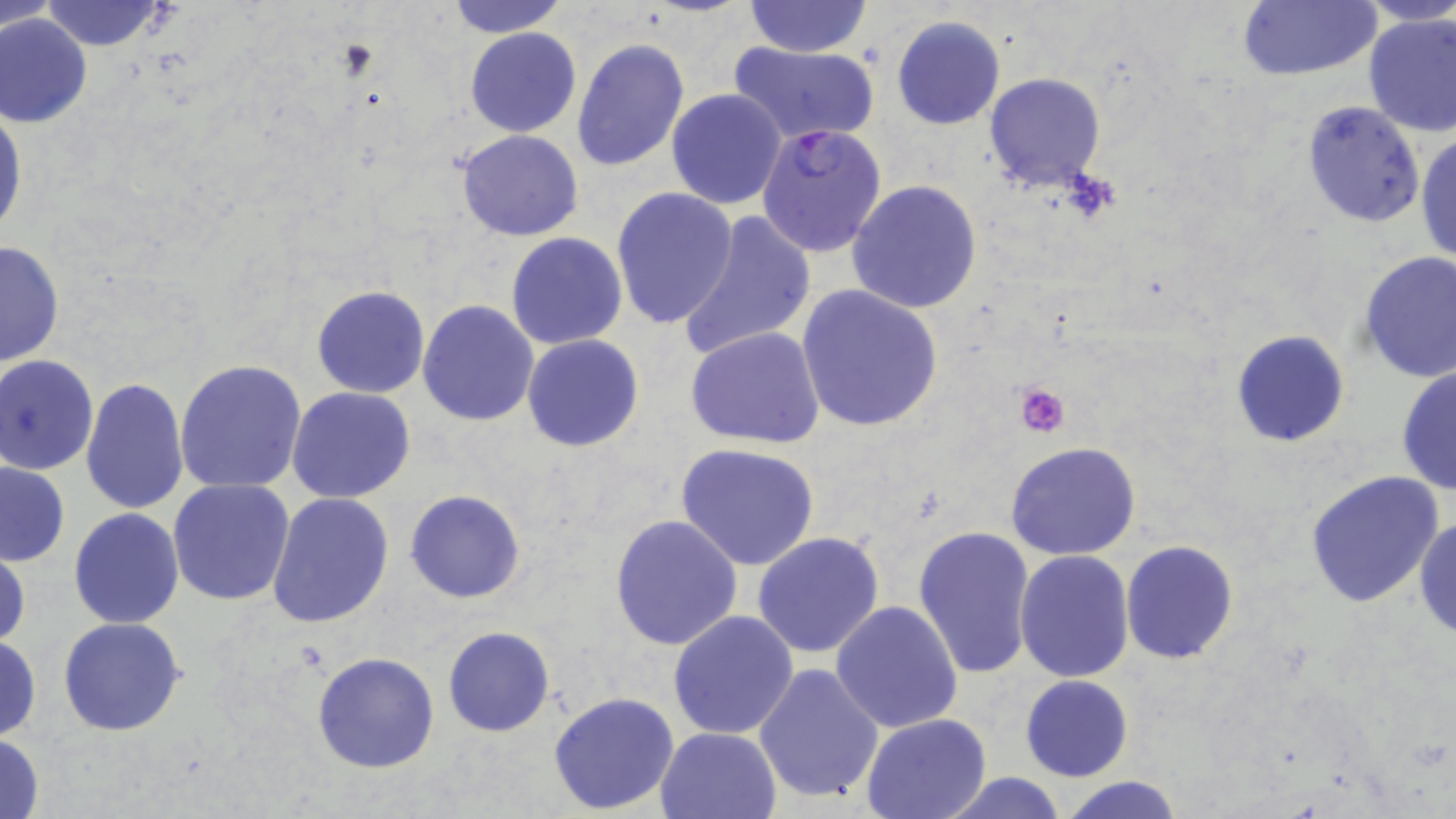
Summary:
  - Coordinate format: approximate bounding boxes as named x1/y1/x2/y2 corners in pixels
  - Uninfected red blood cell locations: (x1=1, y1=0, x2=59, y2=33), (x1=446, y1=0, x2=567, y2=36), (x1=741, y1=0, x2=873, y2=59), (x1=1236, y1=0, x2=1383, y2=80), (x1=1352, y1=0, x2=1455, y2=29), (x1=37, y1=2, x2=171, y2=52), (x1=1361, y1=13, x2=1455, y2=137), (x1=0, y1=14, x2=94, y2=128), (x1=891, y1=15, x2=1005, y2=130), (x1=465, y1=27, x2=581, y2=137), (x1=571, y1=39, x2=690, y2=172), (x1=727, y1=41, x2=880, y2=146), (x1=985, y1=72, x2=1106, y2=190), (x1=666, y1=89, x2=787, y2=209), (x1=1300, y1=99, x2=1425, y2=227), (x1=0, y1=104, x2=27, y2=242), (x1=456, y1=129, x2=584, y2=240), (x1=1416, y1=130, x2=1455, y2=269), (x1=847, y1=179, x2=982, y2=316), (x1=611, y1=186, x2=740, y2=330), (x1=678, y1=212, x2=815, y2=361), (x1=506, y1=232, x2=629, y2=350), (x1=0, y1=240, x2=64, y2=369), (x1=1358, y1=251, x2=1456, y2=382), (x1=312, y1=285, x2=430, y2=399), (x1=798, y1=285, x2=943, y2=433), (x1=417, y1=299, x2=540, y2=426), (x1=684, y1=326, x2=827, y2=449), (x1=1230, y1=328, x2=1351, y2=447), (x1=521, y1=333, x2=644, y2=452), (x1=0, y1=355, x2=99, y2=474), (x1=175, y1=359, x2=308, y2=495), (x1=1395, y1=364, x2=1455, y2=495), (x1=81, y1=378, x2=188, y2=518), (x1=287, y1=387, x2=415, y2=503), (x1=1005, y1=441, x2=1142, y2=561), (x1=676, y1=444, x2=820, y2=572), (x1=1, y1=460, x2=70, y2=565), (x1=1303, y1=472, x2=1447, y2=610), (x1=167, y1=479, x2=296, y2=606), (x1=404, y1=489, x2=524, y2=604), (x1=266, y1=491, x2=395, y2=630), (x1=68, y1=508, x2=185, y2=628), (x1=611, y1=513, x2=744, y2=651), (x1=1414, y1=515, x2=1456, y2=640), (x1=912, y1=524, x2=1038, y2=679), (x1=753, y1=531, x2=886, y2=659), (x1=1120, y1=539, x2=1239, y2=664), (x1=0, y1=541, x2=29, y2=654), (x1=1015, y1=550, x2=1137, y2=683), (x1=830, y1=600, x2=963, y2=736), (x1=668, y1=610, x2=799, y2=740), (x1=59, y1=616, x2=185, y2=735), (x1=442, y1=626, x2=554, y2=737), (x1=0, y1=635, x2=41, y2=743), (x1=311, y1=652, x2=439, y2=773), (x1=752, y1=662, x2=885, y2=806), (x1=1020, y1=675, x2=1133, y2=782), (x1=548, y1=691, x2=680, y2=812), (x1=862, y1=714, x2=991, y2=819), (x1=656, y1=726, x2=782, y2=818), (x1=0, y1=733, x2=47, y2=817), (x1=933, y1=772, x2=1074, y2=818), (x1=1056, y1=774, x2=1185, y2=818)
  - Platelet locations: (x1=1014, y1=382, x2=1071, y2=439)
  - Plasmodium falciparum-infected red blood cell locations: (x1=756, y1=122, x2=888, y2=257)
  - Slide-level diagnosis: Plasmodium falciparum
  - Modality: light microscopy
  - Field of view: single
  - Magnification: 1000x
  - Preparation: thin blood smear
  - Image size: 1456×819 pixels
  - Stain: May-Grünwald-Giemsa